Classify this cell by malaria status.
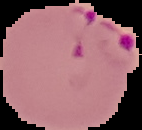

It is parasitized.

Summary:
  - Image type: cell region segmented out of the field of view; surrounding area masked to black
  - Preparation: thin blood film
  - Image size: 142×130 pixels